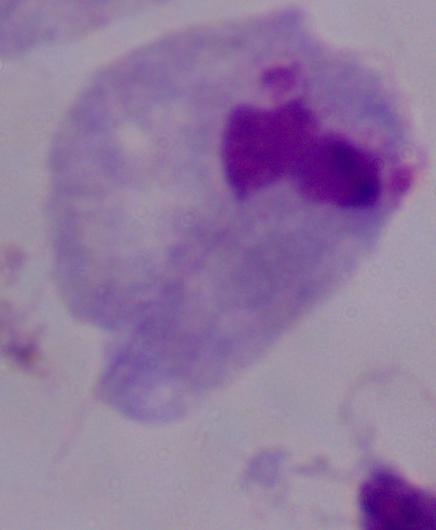

A trichomonad is seen. 1000x magnification. Photomicrograph.